Mark where leukocytes are.
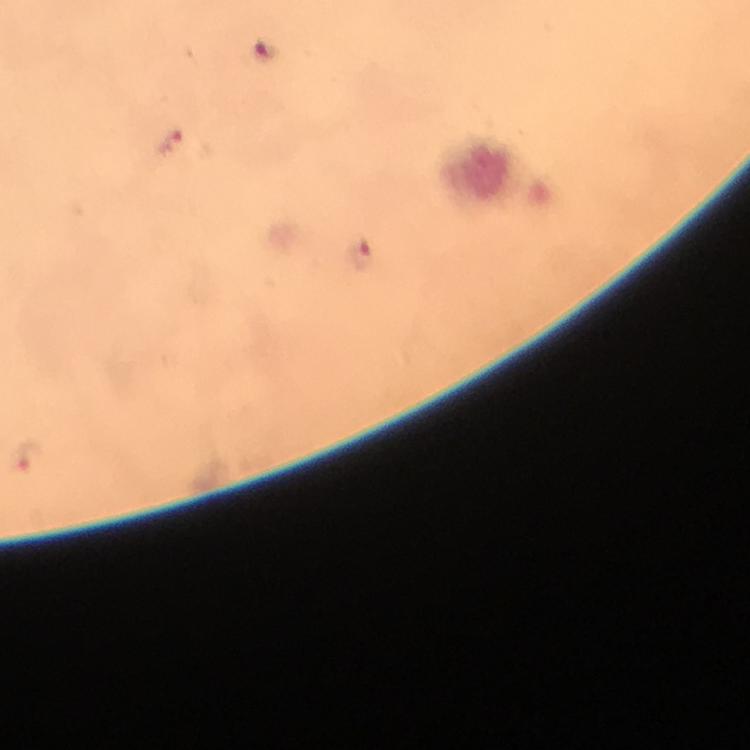
Approximate centers as [x, y] in pixels.
Leukocytes: [493, 174].

Plasmodium parasite locations: [170, 143], [362, 255], [28, 457]. Image is 750×750 pixels. Photographed with a smartphone mounted on the microscope. Giemsa stain. From a malaria diagnostic workup. Thick blood film. Cropped region of a single field of view. 100x magnification. Immersion oil was used.